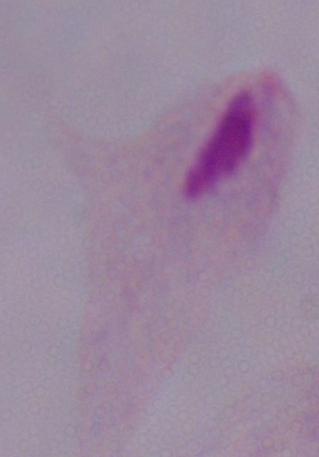
modality: photomicrograph
identification: trichomonad
magnification: 1000x